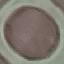

Summary:
  - Malaria status: uninfected
  - Capture: smartphone through the microscope eyepiece
  - Image type: automatically extracted cell patch, resized to 64 × 64 pixels
  - Stain: Giemsa
  - Preparation: thin blood film